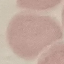
Result: no malaria parasites detected. Thin blood film. Photographed with a smartphone camera at the microscope eyepiece. Automatically extracted cell patch, resized to 64 × 64 pixels. Giemsa-stained preparation.